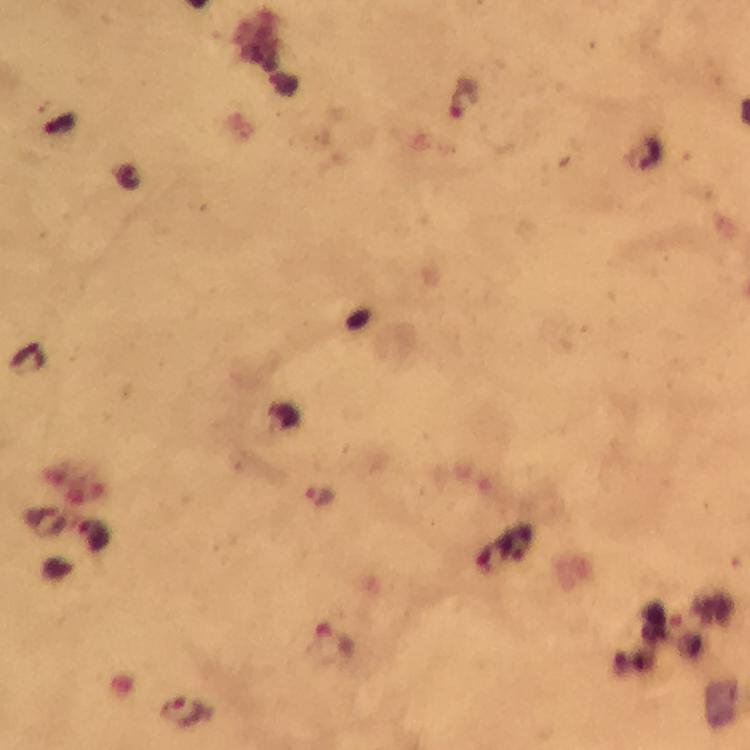
{
  "plasmodium_parasite_locations": "approximate object centers, in pixels from the top-left corner: (x=319, y=498), (x=334, y=640), (x=180, y=712)",
  "capture": "smartphone photograph through a microscope",
  "magnification": "100x",
  "cropped_from": "a single field of view",
  "image_size": "750×750 pixels",
  "stain": "Giemsa",
  "context": "from a malaria diagnostic workup",
  "preparation": "thick smear",
  "immersion_oil": "applied"
}